State the blood parasite species.
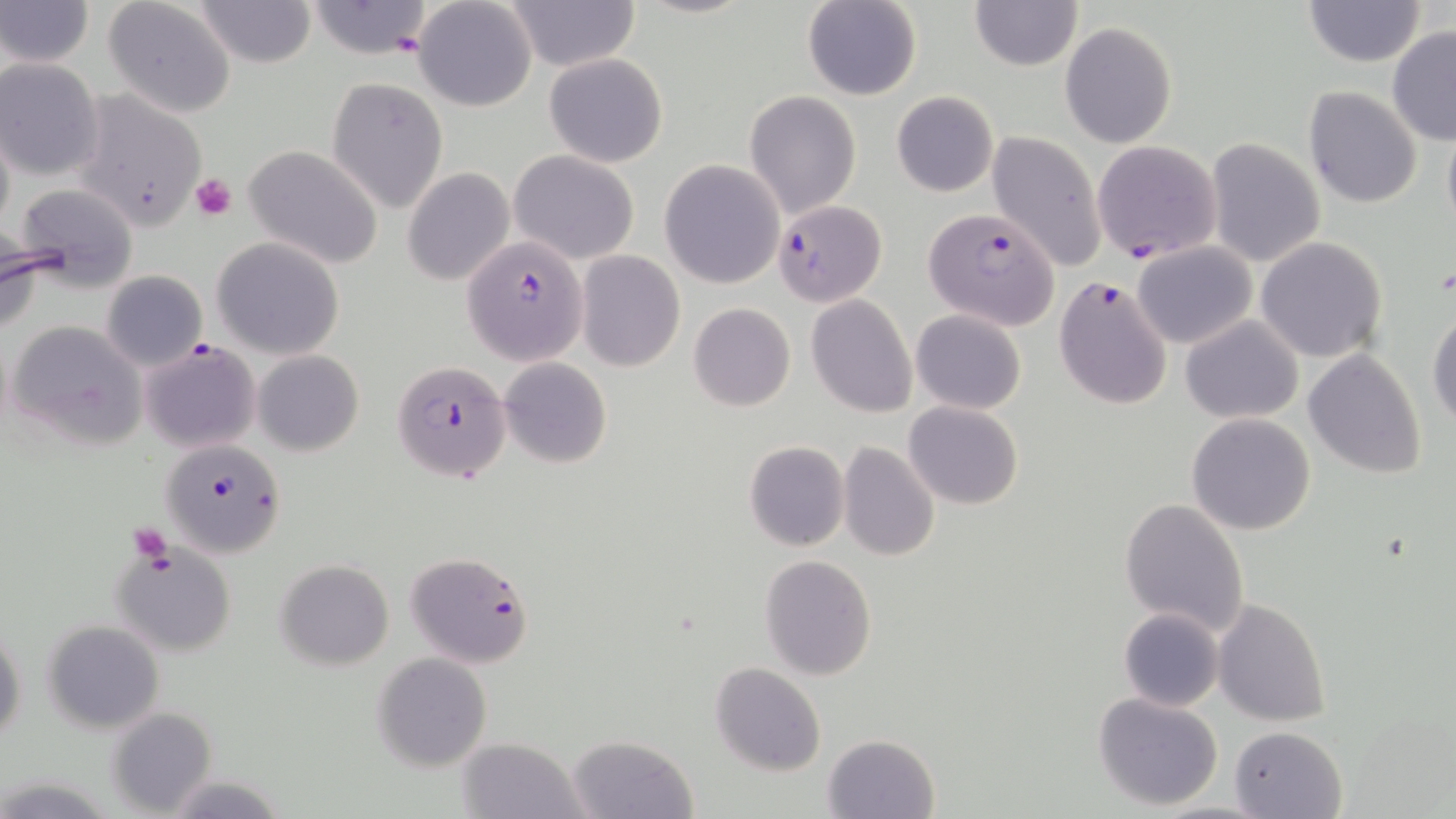
Plasmodium falciparum.

modality = optical microscopy
uninfected red blood cell locations = approximate bounding boxes as (x1, y1, x2, y2) in pixels: (2, 0, 93, 68), (103, 0, 237, 118), (193, 0, 317, 69), (413, 0, 538, 112), (1303, 0, 1427, 67), (306, 1, 435, 60), (500, 1, 639, 71), (801, 1, 922, 101), (970, 1, 1082, 72), (1061, 22, 1177, 147), (1386, 26, 1456, 147), (543, 53, 668, 168), (1, 58, 105, 181), (327, 75, 449, 213), (1303, 86, 1423, 208), (745, 90, 863, 216), (890, 90, 998, 197), (67, 91, 210, 234), (1442, 114, 1456, 241), (0, 116, 14, 240), (986, 131, 1107, 271), (1205, 139, 1326, 267), (245, 146, 383, 269), (509, 149, 640, 264), (659, 160, 785, 289), (402, 168, 515, 286), (10, 181, 143, 291), (1, 236, 56, 333), (212, 236, 345, 360), (1255, 237, 1388, 363), (1133, 243, 1256, 349), (576, 251, 684, 371), (101, 271, 208, 371), (807, 295, 917, 419), (688, 302, 796, 412), (1427, 308, 1456, 430), (912, 310, 1025, 414), (1181, 314, 1305, 424), (8, 319, 146, 448), (1304, 349, 1427, 478), (253, 350, 364, 457), (499, 358, 612, 469), (904, 400, 1023, 510), (1187, 413, 1315, 535), (743, 440, 849, 552), (838, 442, 940, 562), (1120, 497, 1250, 637), (113, 542, 238, 658), (759, 554, 878, 680), (277, 560, 394, 669), (1212, 597, 1331, 726), (1118, 607, 1224, 712), (42, 620, 164, 733), (1, 629, 25, 744), (372, 653, 492, 771), (711, 662, 825, 776), (1092, 691, 1224, 809), (107, 708, 215, 816), (1230, 726, 1346, 817), (566, 734, 697, 818), (824, 734, 943, 819), (459, 735, 587, 819), (165, 775, 285, 817), (4, 778, 115, 815)
image size = 1456×819 pixels
preparation = thin blood film
magnification = 1000x
stain = May-Grünwald-Giemsa
platelet locations = approximate bounding boxes as (x1, y1, x2, y2) in pixels: (190, 173, 238, 221), (127, 523, 174, 566)
Plasmodium falciparum-infected red blood cell locations = approximate bounding boxes as (x1, y1, x2, y2) in pixels: (1091, 140, 1222, 262), (774, 198, 887, 307), (922, 208, 1061, 331), (463, 236, 588, 364), (1054, 275, 1173, 409), (141, 339, 260, 452), (392, 359, 511, 484), (160, 439, 287, 558), (404, 551, 533, 669)
field of view = one of a larger specimen